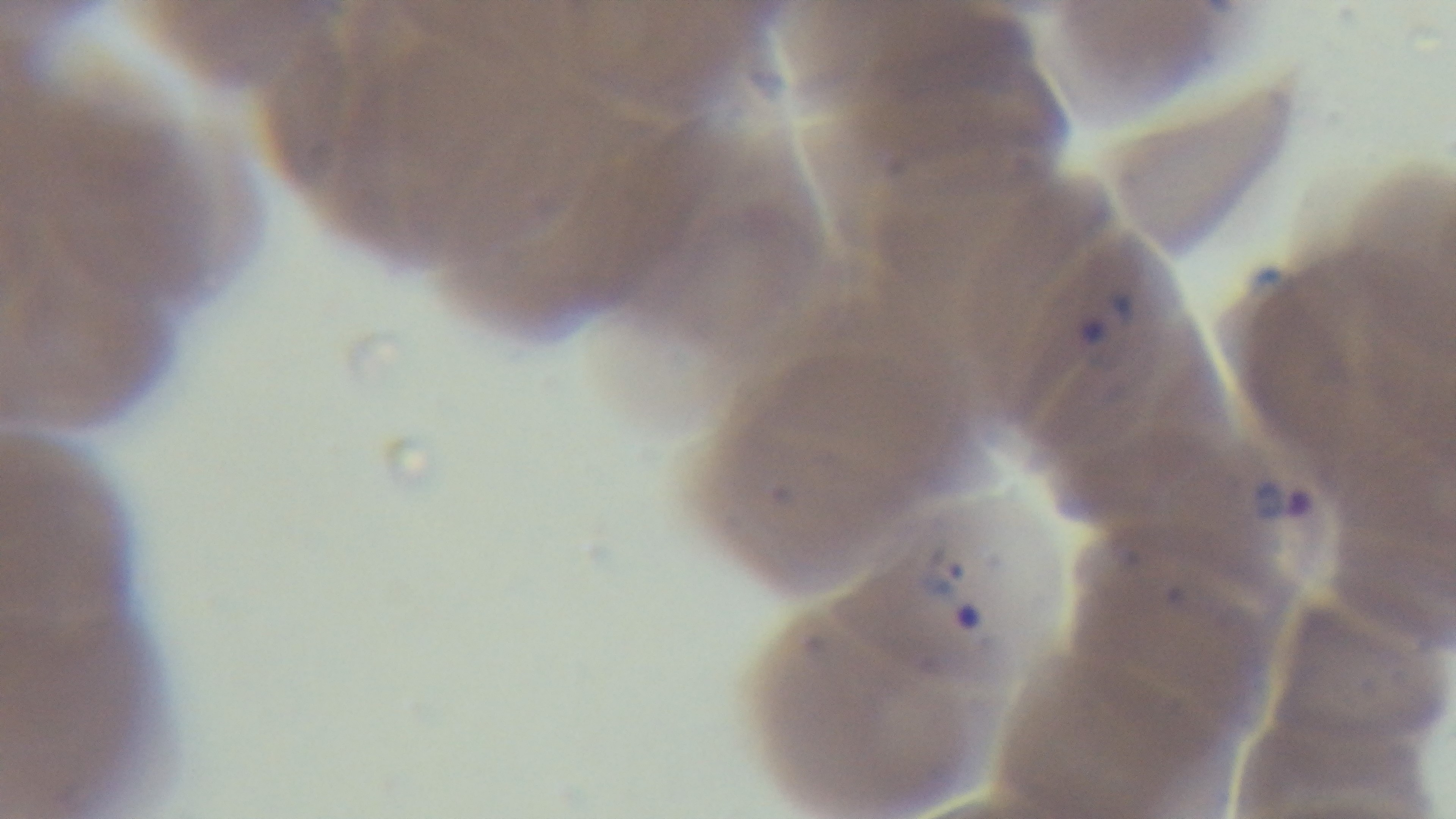
Malaria status: infected. Preparation: thin smear. 100x oil-immersion objective. Giemsa-stained. One field from the slide. Photomicrograph. Captured with a mounted 4K digital camera.